Outline each blood parasite and name the species.
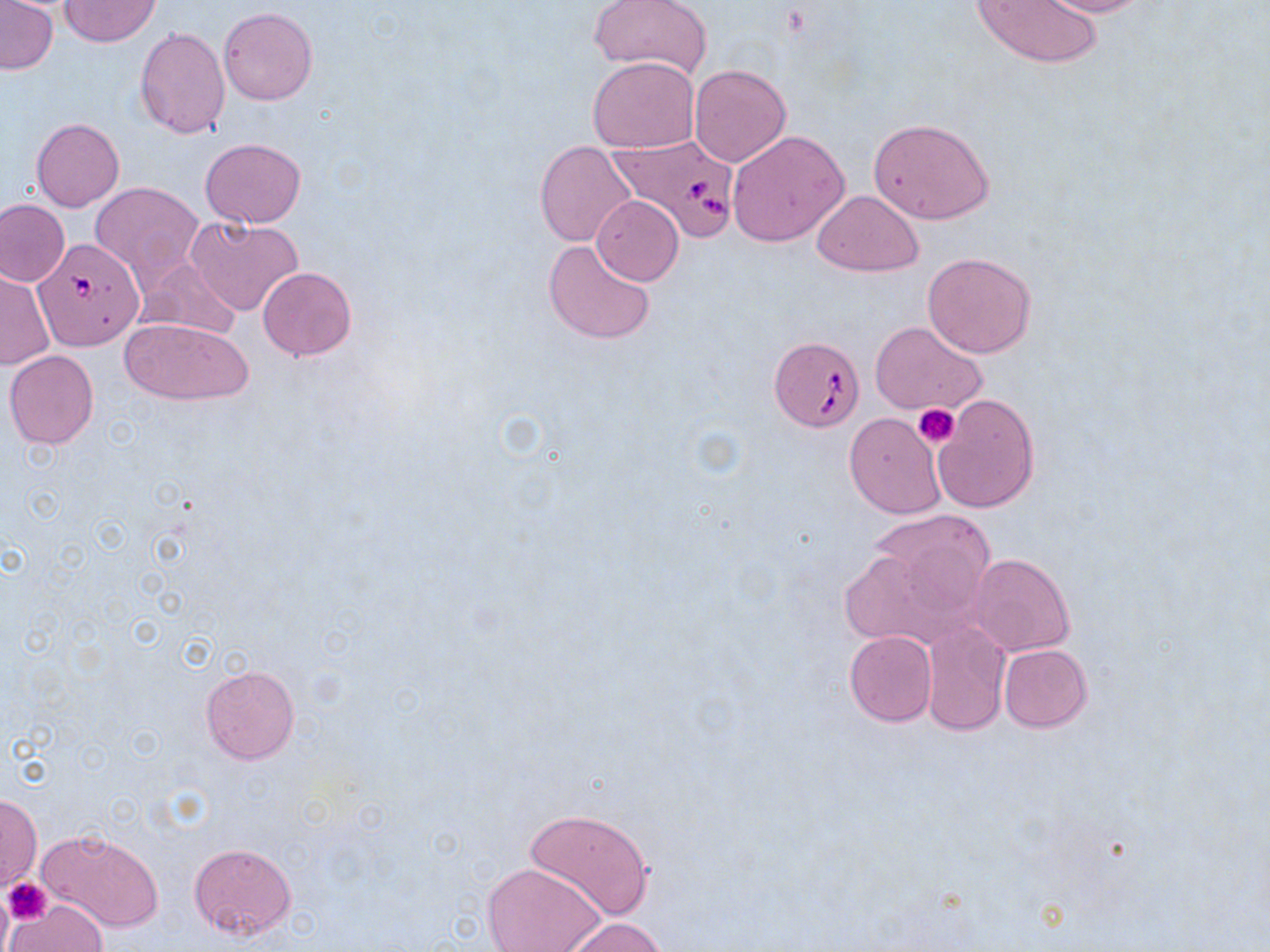

Approximate bounding boxes as named x1/y1/x2/y2 corners in pixels.
Babesia divergens-infected red blood cells: (x1=605, y1=134, x2=743, y2=241), (x1=35, y1=239, x2=144, y2=350), (x1=768, y1=335, x2=863, y2=432).
No Plasmodium falciparum, Plasmodium ovale, Plasmodium malariae, Plasmodium vivax, or Trypanosoma brucei observed.

Platelet locations: (x1=914, y1=403, x2=960, y2=448), (x1=3, y1=877, x2=51, y2=924). Uninfected red blood cell locations: (x1=59, y1=0, x2=160, y2=46), (x1=971, y1=0, x2=1103, y2=69), (x1=1035, y1=0, x2=1152, y2=18), (x1=0, y1=1, x2=58, y2=75), (x1=592, y1=1, x2=709, y2=76), (x1=219, y1=8, x2=317, y2=105), (x1=134, y1=27, x2=231, y2=139), (x1=587, y1=57, x2=699, y2=153), (x1=688, y1=64, x2=791, y2=165), (x1=867, y1=116, x2=995, y2=225), (x1=32, y1=118, x2=124, y2=211), (x1=727, y1=130, x2=849, y2=246), (x1=200, y1=139, x2=306, y2=227), (x1=536, y1=141, x2=637, y2=246), (x1=91, y1=182, x2=204, y2=282), (x1=812, y1=191, x2=924, y2=275), (x1=592, y1=196, x2=684, y2=285), (x1=0, y1=199, x2=69, y2=287), (x1=185, y1=216, x2=303, y2=316), (x1=542, y1=240, x2=657, y2=345), (x1=922, y1=252, x2=1037, y2=358), (x1=133, y1=259, x2=244, y2=341), (x1=258, y1=266, x2=356, y2=361), (x1=0, y1=267, x2=54, y2=369), (x1=120, y1=316, x2=254, y2=406), (x1=870, y1=320, x2=987, y2=419), (x1=4, y1=350, x2=99, y2=449), (x1=932, y1=394, x2=1040, y2=513), (x1=844, y1=412, x2=947, y2=519), (x1=846, y1=510, x2=998, y2=645), (x1=967, y1=553, x2=1076, y2=657), (x1=921, y1=622, x2=1010, y2=736), (x1=845, y1=631, x2=937, y2=726), (x1=998, y1=644, x2=1091, y2=731), (x1=199, y1=664, x2=299, y2=764), (x1=1, y1=794, x2=41, y2=891), (x1=523, y1=806, x2=654, y2=920), (x1=39, y1=829, x2=164, y2=933), (x1=189, y1=843, x2=297, y2=943), (x1=482, y1=860, x2=605, y2=952), (x1=6, y1=899, x2=106, y2=952), (x1=559, y1=916, x2=666, y2=952). Slide-level diagnosis: Babesia divergens. May-Grünwald-Giemsa-stained preparation. Captured at 1000x magnification. One field of a larger specimen. Optical microscopy. Thin blood film. Image is 1270×952 pixels.